Locate every blood parasite and identify its species.
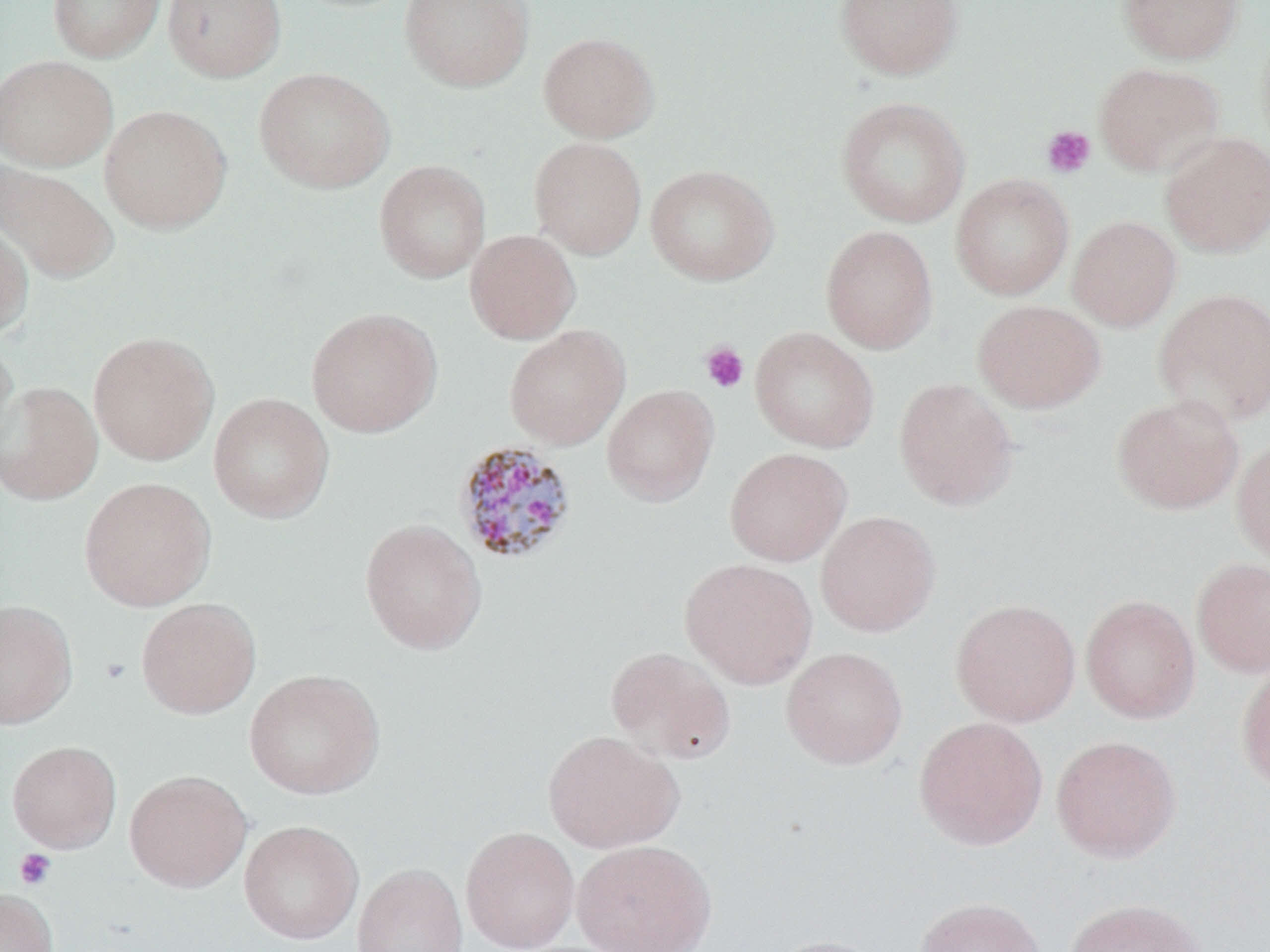
Approximate bounding boxes as named x1/y1/x2/y2 corners in pixels.
Plasmodium malariae-infected red blood cells: (x1=452, y1=440, x2=579, y2=567).
No Plasmodium falciparum, Plasmodium ovale, Plasmodium vivax, Babesia divergens, or Trypanosoma brucei observed.

slide-level diagnosis = Plasmodium malariae
modality = optical microscopy
image size = 1270×952 pixels
magnification = 1000x
platelet locations = approximate bounding boxes as named x1/y1/x2/y2 corners in pixels: (x1=1041, y1=125, x2=1096, y2=178), (x1=699, y1=341, x2=749, y2=393), (x1=100, y1=657, x2=131, y2=684), (x1=14, y1=848, x2=57, y2=890)
field of view = one of a larger specimen
preparation = thin blood smear
stain = May-Grünwald-Giemsa
uninfected red blood cell locations = approximate bounding boxes as named x1/y1/x2/y2 corners in pixels: (x1=48, y1=0, x2=165, y2=63), (x1=162, y1=0, x2=286, y2=82), (x1=399, y1=0, x2=534, y2=92), (x1=834, y1=0, x2=965, y2=80), (x1=1116, y1=0, x2=1244, y2=64), (x1=1255, y1=24, x2=1270, y2=158), (x1=538, y1=32, x2=660, y2=142), (x1=0, y1=55, x2=117, y2=171), (x1=1093, y1=62, x2=1225, y2=177), (x1=253, y1=67, x2=395, y2=194), (x1=835, y1=96, x2=970, y2=229), (x1=98, y1=104, x2=232, y2=234), (x1=1159, y1=131, x2=1270, y2=258), (x1=528, y1=137, x2=647, y2=260), (x1=373, y1=159, x2=491, y2=284), (x1=0, y1=160, x2=119, y2=284), (x1=645, y1=164, x2=780, y2=286), (x1=950, y1=174, x2=1074, y2=300), (x1=1067, y1=215, x2=1182, y2=332), (x1=0, y1=221, x2=34, y2=341), (x1=821, y1=225, x2=938, y2=355), (x1=465, y1=229, x2=581, y2=344), (x1=1153, y1=287, x2=1270, y2=426), (x1=972, y1=299, x2=1106, y2=413), (x1=305, y1=307, x2=443, y2=438), (x1=504, y1=324, x2=631, y2=450), (x1=749, y1=327, x2=880, y2=453), (x1=88, y1=330, x2=220, y2=466), (x1=0, y1=335, x2=21, y2=467), (x1=893, y1=378, x2=1019, y2=510), (x1=0, y1=381, x2=103, y2=506), (x1=602, y1=384, x2=719, y2=507), (x1=207, y1=392, x2=335, y2=523), (x1=1111, y1=393, x2=1244, y2=515), (x1=1232, y1=436, x2=1270, y2=569), (x1=724, y1=447, x2=852, y2=567), (x1=78, y1=476, x2=217, y2=612), (x1=815, y1=510, x2=940, y2=637), (x1=359, y1=518, x2=487, y2=655), (x1=1191, y1=557, x2=1270, y2=677), (x1=679, y1=558, x2=818, y2=689), (x1=1081, y1=594, x2=1201, y2=723), (x1=136, y1=597, x2=261, y2=719), (x1=950, y1=598, x2=1081, y2=726), (x1=0, y1=599, x2=78, y2=729), (x1=606, y1=646, x2=736, y2=764), (x1=780, y1=646, x2=908, y2=769), (x1=1236, y1=658, x2=1270, y2=794), (x1=244, y1=668, x2=385, y2=800), (x1=913, y1=716, x2=1048, y2=851), (x1=543, y1=729, x2=685, y2=853), (x1=1051, y1=734, x2=1181, y2=861), (x1=6, y1=740, x2=122, y2=853), (x1=124, y1=769, x2=252, y2=892), (x1=239, y1=820, x2=363, y2=944), (x1=460, y1=826, x2=580, y2=952), (x1=571, y1=838, x2=717, y2=952), (x1=352, y1=861, x2=469, y2=952), (x1=0, y1=887, x2=58, y2=952), (x1=915, y1=896, x2=1045, y2=952), (x1=1064, y1=898, x2=1208, y2=952), (x1=765, y1=934, x2=887, y2=952)